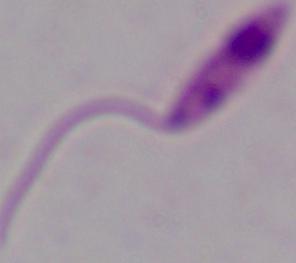
modality: photomicrograph
magnification: 1000x
identification: Leishmania